Point out each malaria parasite and each leukocyte.
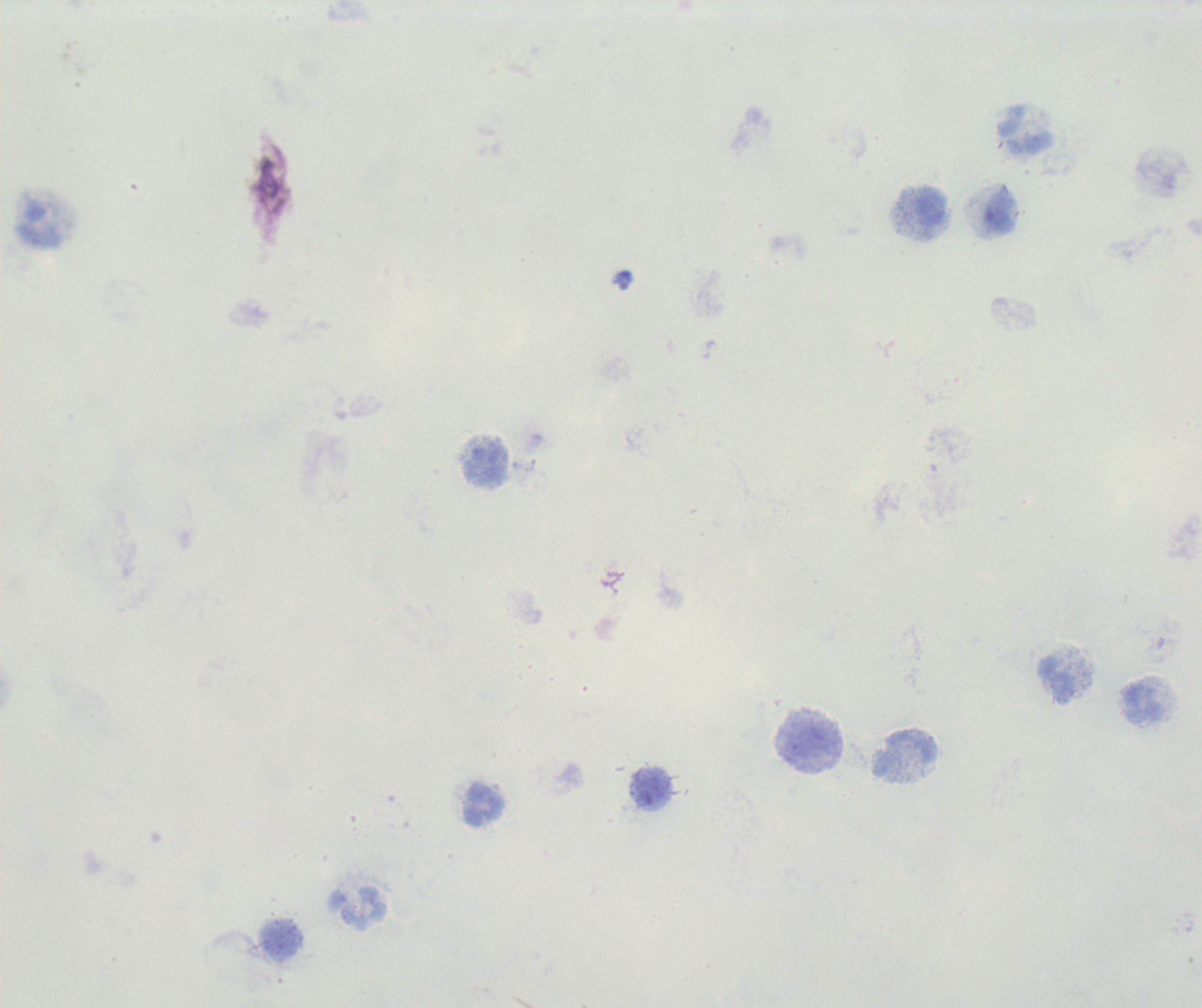
No malaria parasites detected.
Approximate object centers, in pixels from the top-left corner.
Leukocytes: (x=1027, y=130), (x=930, y=205), (x=1000, y=211), (x=40, y=225), (x=1056, y=680), (x=1144, y=701), (x=809, y=740), (x=905, y=753), (x=652, y=788), (x=484, y=805), (x=357, y=907), (x=280, y=938).

preparation = thick blood film
stain = Romanowsky
image size = 1202×1008 pixels
magnification = 100x
background quality = poor
field of view = one from this slide
context = previously used in an actual diagnosis